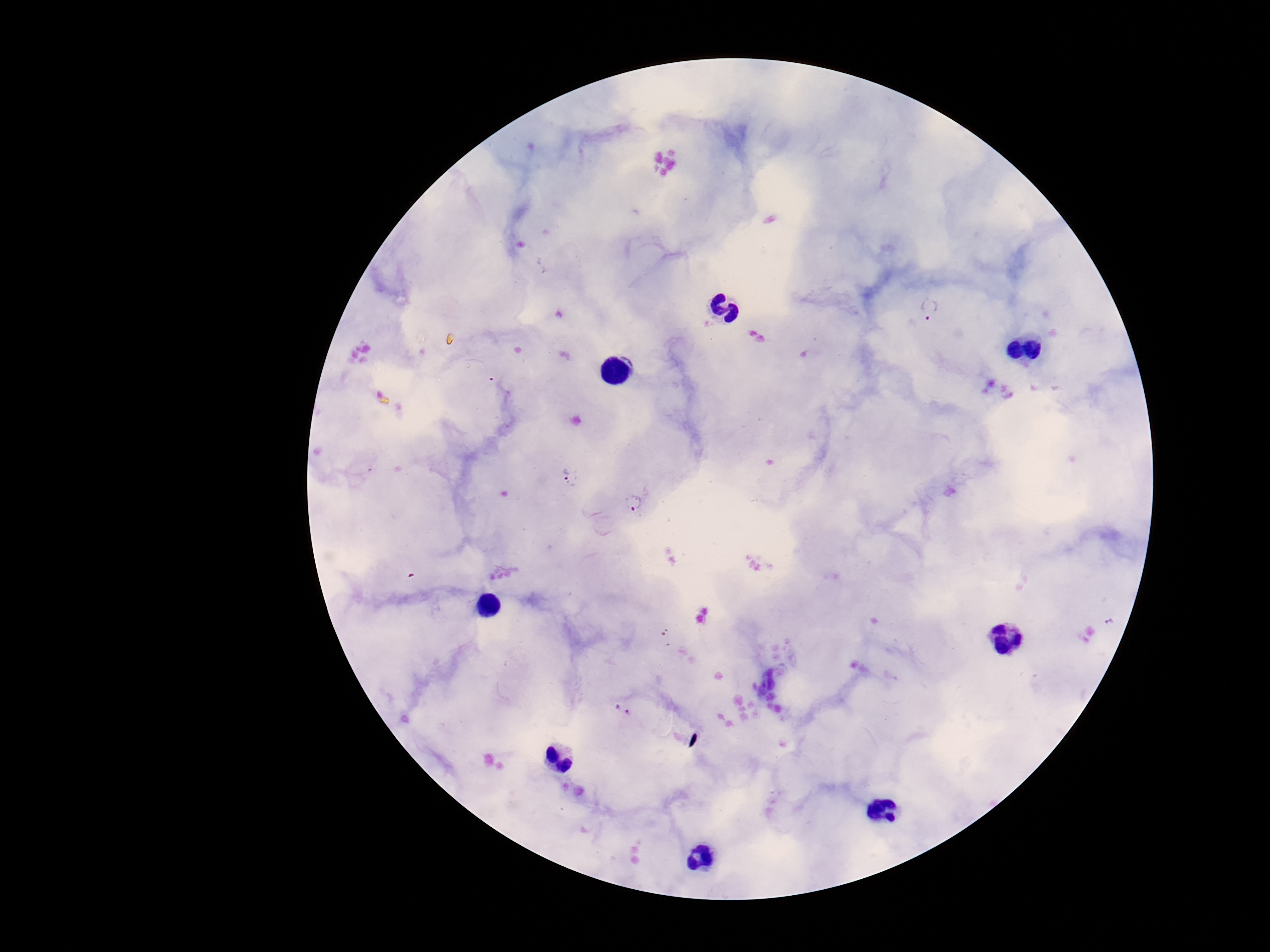
image size = 1270×952 pixels
preparation = thick blood film
stain = Giemsa
Plasmodium parasite locations = approximate centers as (x, y) in pixels: (929, 312), (569, 477), (633, 503), (623, 710)
field of view = single
patient malaria status = infected
capture = smartphone camera through the microscope eyepiece
magnification = 100x